State the preparation type.
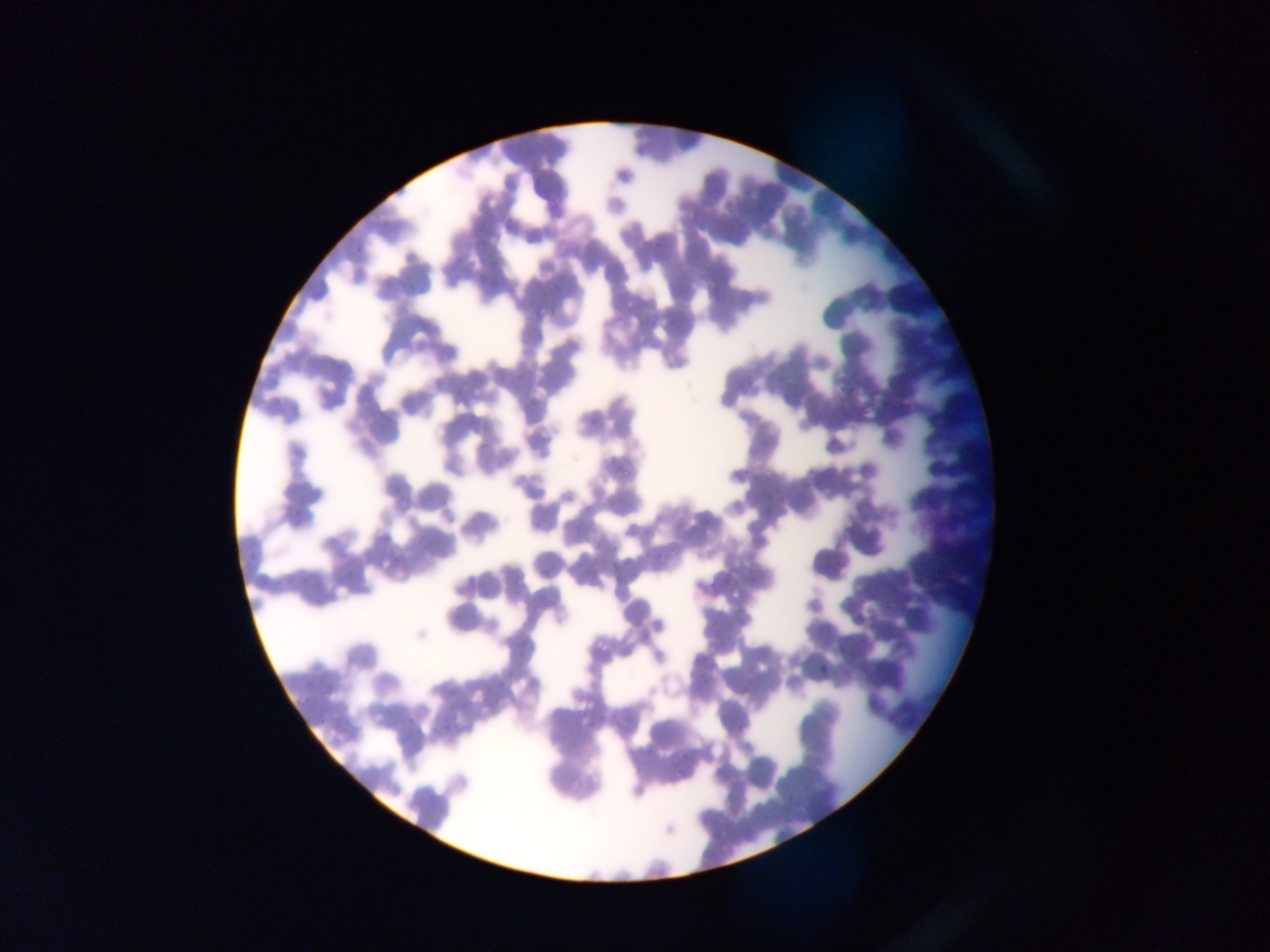
This is a thin smear.

Approximate bounding boxes as left top right bottom in pixels.
Summary:
  - Plasmodium parasite locations: 620 464 632 478; 654 546 668 560; 513 573 528 587; 815 663 827 675; 578 704 587 716
  - Field of view: single
  - Country: Ghana
  - Image size: 1270×952 pixels
  - Capture: mobile-phone photograph through a microscope